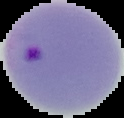
Summary:
  - Image type: cell region segmented out of the field of view; surrounding area masked to black
  - Malaria status: parasitized
  - Preparation: thin blood film
  - Image size: 124×118 pixels